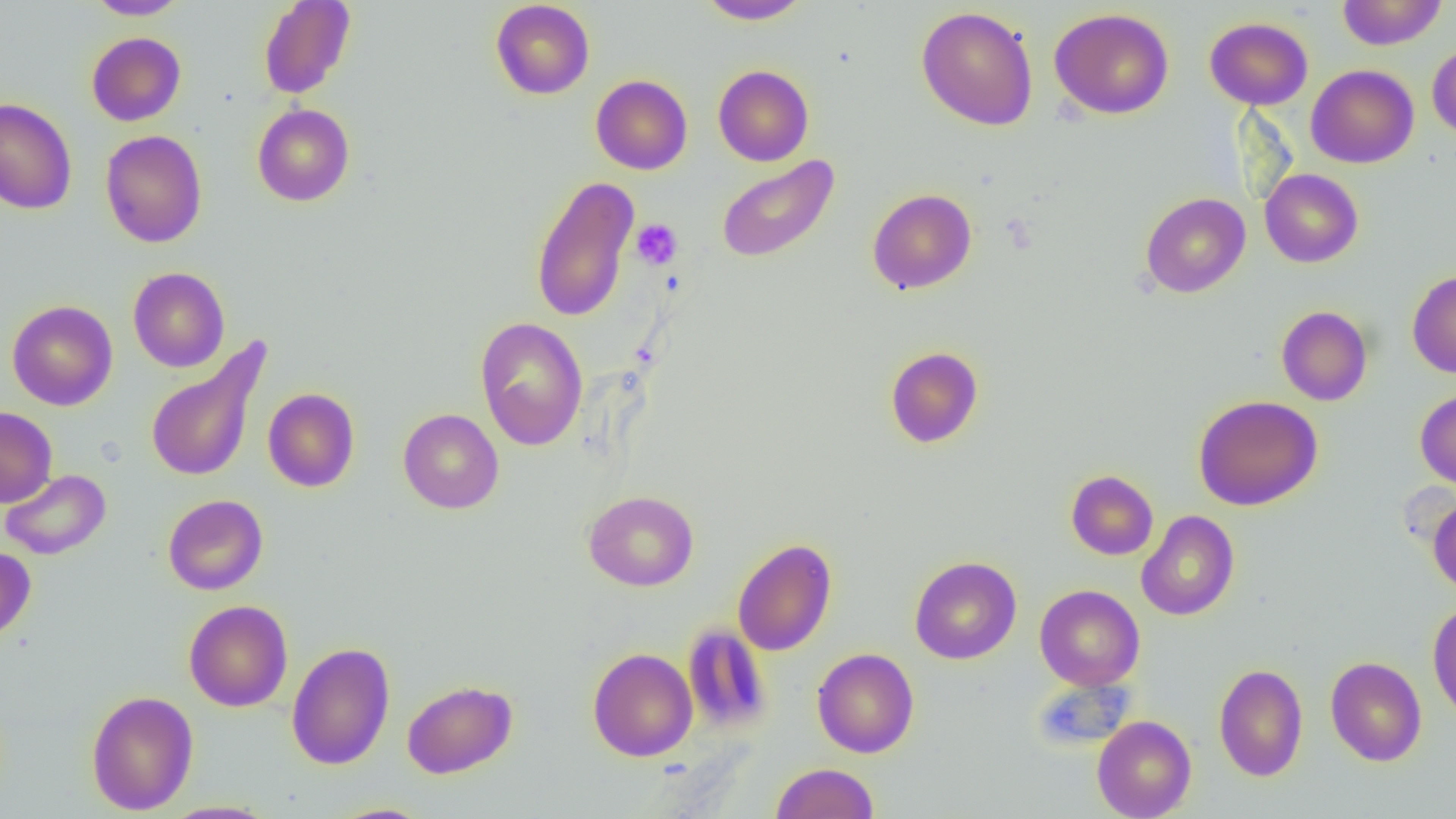
Summary:
  - Coordinate format: approximate bounding boxes as (x1,y1)-(x2,y2) corner pairs in pixels
  - Uninfected red blood cell locations: (86,0)-(189,19), (258,0)-(355,99), (490,0)-(595,100), (696,0)-(811,25), (1337,0)-(1448,49), (916,6)-(1038,130), (1049,8)-(1174,119), (1204,17)-(1313,110), (86,32)-(186,126), (1427,43)-(1456,140), (1306,64)-(1419,168), (713,65)-(814,166), (591,74)-(692,174), (0,98)-(77,214), (252,103)-(355,206), (100,129)-(207,248), (716,156)-(839,263), (1260,168)-(1363,268), (530,174)-(640,323), (867,188)-(977,294), (1140,192)-(1251,298), (128,267)-(230,372), (1407,269)-(1456,379), (7,300)-(117,410), (1276,306)-(1372,406), (475,317)-(589,451), (145,340)-(271,484), (884,346)-(984,449), (262,388)-(360,492), (1415,389)-(1456,491), (1193,394)-(1323,511), (0,406)-(57,507), (398,408)-(504,513), (1,469)-(111,560), (1066,470)-(1158,560), (583,491)-(699,591), (163,494)-(268,594), (1427,495)-(1456,595), (1136,511)-(1239,620), (732,538)-(837,656), (0,546)-(36,643), (909,555)-(1022,664), (1034,584)-(1145,690), (184,600)-(293,712), (1427,600)-(1456,724), (682,623)-(771,733), (286,642)-(395,770), (587,648)-(698,761), (812,648)-(919,758), (1325,656)-(1427,766), (1214,662)-(1307,782), (402,679)-(518,779), (85,690)-(199,815), (1092,715)-(1196,819), (770,762)-(879,819), (161,801)-(278,818), (323,803)-(436,819)
  - Platelet locations: (631,219)-(682,269)
  - Slide-level diagnosis: no evidence of blood parasites
  - Magnification: 1000x
  - Modality: light microscopy
  - Image size: 1456×819 pixels
  - Field of view: one of a larger specimen
  - Preparation: thin blood smear